Locate every blood parasite and identify its species.
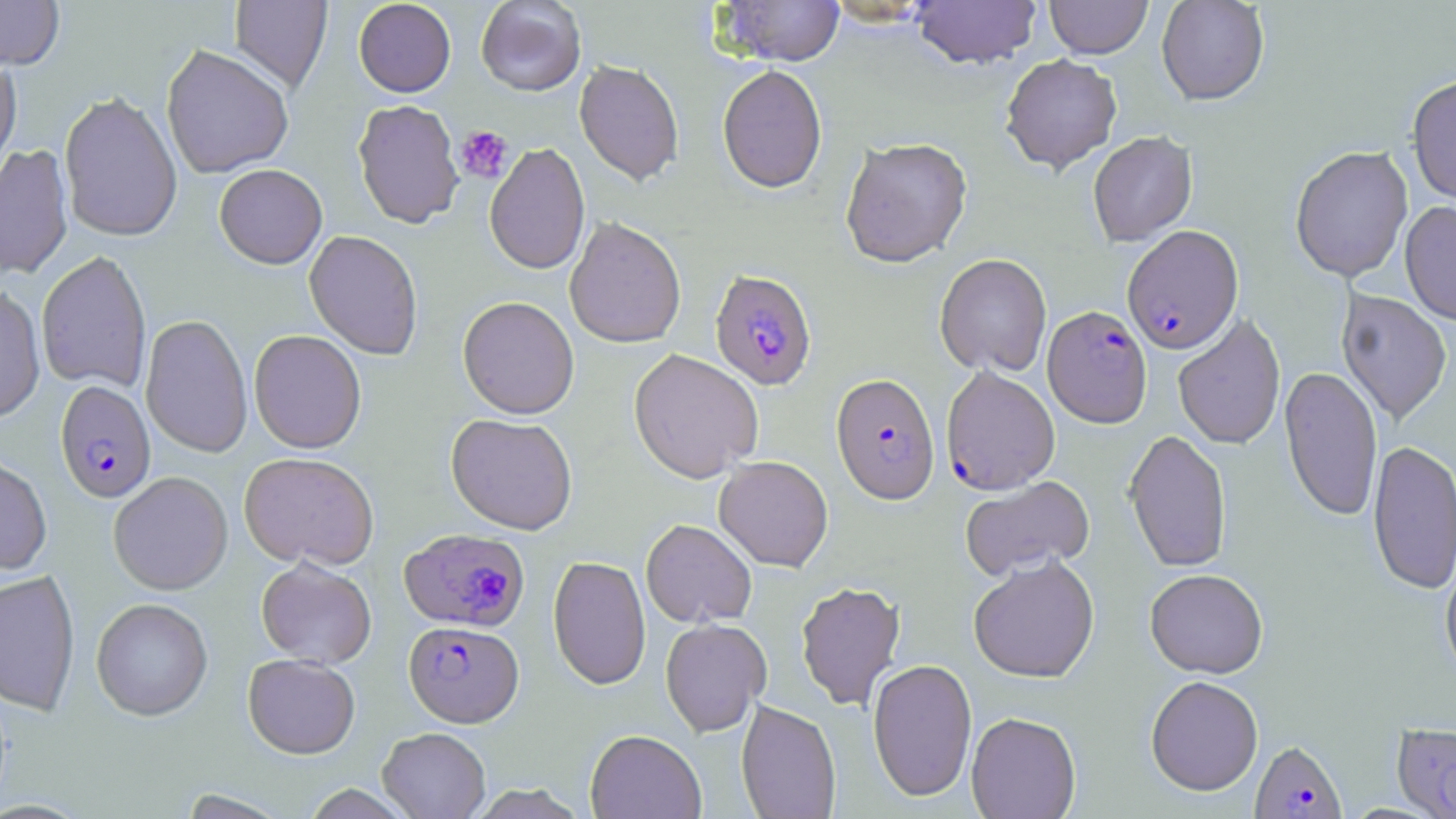

Approximate bounding boxes as [x1, y1, x2, y2] in pixels.
Plasmodium falciparum-infected red blood cells: [1122, 224, 1243, 354], [710, 269, 817, 390], [1042, 305, 1152, 427], [940, 365, 1060, 495], [831, 372, 939, 504], [55, 380, 156, 503], [399, 528, 529, 632], [404, 620, 523, 727], [1394, 723, 1456, 815], [1250, 740, 1347, 818].
No Plasmodium ovale, Plasmodium malariae, Plasmodium vivax, Babesia divergens, or Trypanosoma brucei observed.

Summary:
  - Uninfected red blood cell locations: [0, 0, 65, 69], [230, 0, 332, 93], [353, 0, 456, 97], [476, 0, 586, 95], [716, 0, 845, 66], [911, 0, 1041, 69], [1045, 0, 1152, 59], [1156, 0, 1270, 105], [161, 43, 294, 179], [1000, 53, 1122, 173], [0, 54, 22, 181], [574, 59, 684, 186], [717, 64, 828, 193], [1407, 75, 1456, 206], [58, 91, 183, 242], [352, 99, 464, 229], [1087, 131, 1198, 247], [840, 136, 973, 268], [0, 143, 73, 280], [484, 143, 590, 275], [1290, 146, 1413, 281], [214, 164, 327, 268], [1400, 200, 1456, 324], [564, 216, 686, 349], [304, 230, 424, 359], [36, 250, 152, 393], [935, 253, 1052, 377], [0, 285, 46, 423], [1336, 289, 1452, 425], [457, 296, 579, 419], [140, 313, 253, 458], [1173, 314, 1286, 450], [249, 330, 366, 453], [628, 349, 764, 483], [1280, 365, 1383, 522], [446, 413, 578, 535], [1124, 429, 1232, 572], [1367, 439, 1456, 595], [239, 452, 379, 570], [0, 455, 52, 575], [714, 455, 833, 572], [108, 471, 233, 595], [105, 472, 222, 724], [959, 476, 1095, 581], [641, 519, 757, 628], [968, 555, 1100, 683], [548, 556, 651, 690], [256, 557, 377, 668], [1440, 557, 1456, 686], [0, 568, 80, 715], [1145, 568, 1268, 678], [796, 581, 905, 710], [91, 597, 213, 720], [660, 618, 771, 736], [243, 653, 360, 759], [867, 658, 977, 801], [1145, 675, 1263, 796], [736, 700, 841, 819], [966, 711, 1081, 819], [377, 727, 491, 818], [585, 729, 706, 819], [302, 784, 415, 818]
  - Platelet locations: [454, 125, 513, 184]
  - Slide-level diagnosis: Plasmodium falciparum
  - Magnification: 1000x
  - Field of view: single
  - Image size: 1456×819 pixels
  - Stain: May-Grünwald-Giemsa
  - Preparation: thin blood smear
  - Modality: optical microscopy